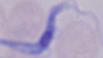

Summary:
  - Identification: trypanosome
  - Modality: micrograph
  - Magnification: 1000x